Comment on the morphology of the erythrocytes.
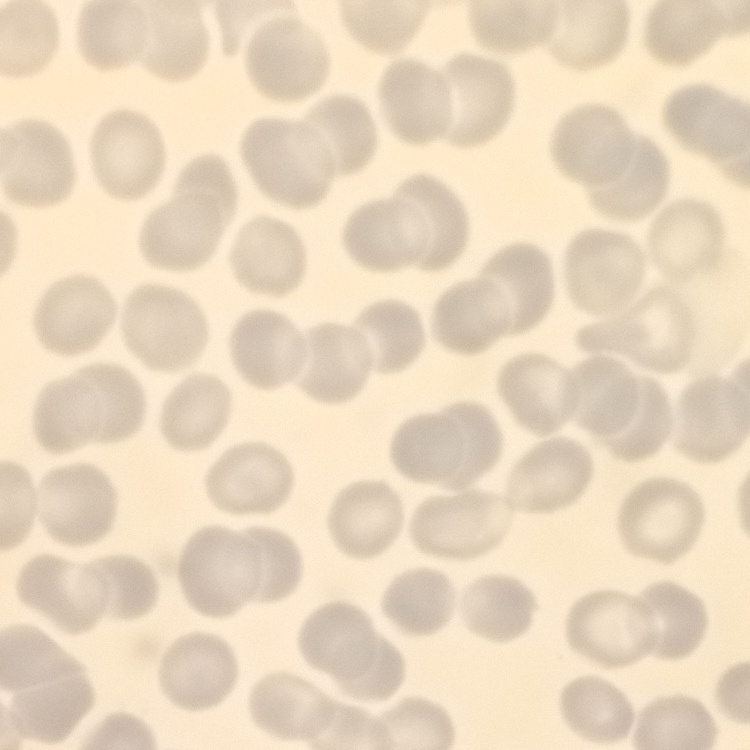
No rouleaux formation.

Thin peripheral smear. Square crop of a larger photomicrograph. Stained with either Field's or Giemsa.